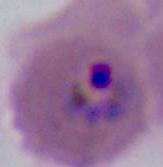
Summary:
  - Modality: micrograph
  - Magnification: 400x or 1000x
  - Identification: Plasmodium